Name the parasite shown.
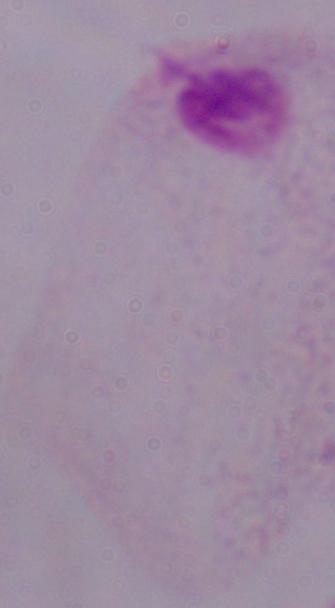
A trichomonad.

Summary:
  - Modality: photomicrograph
  - Magnification: 1000x